Assess the morphology of the red blood cells.
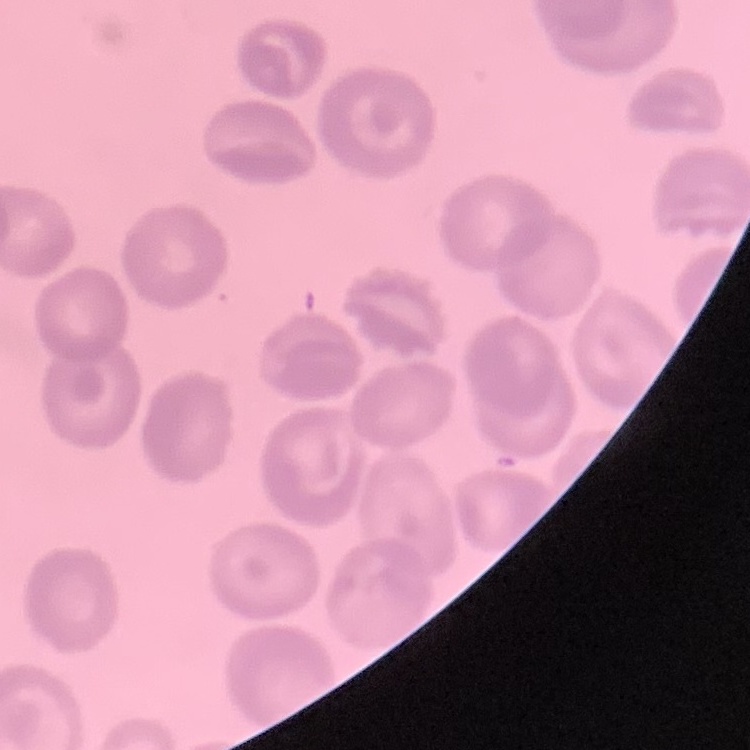

They show no rouleaux formation.

Stained with either Field's or Giemsa. Thin blood smear. One tile cut from a larger photomicrograph.